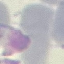

Malaria status: uninfected. Thin blood smear. Giemsa stain. Acquired by smartphone through the microscope eyepiece. Cell patch, automatically extracted from a larger field of view and resized to 64 × 64 pixels.